State which parasite is depicted.
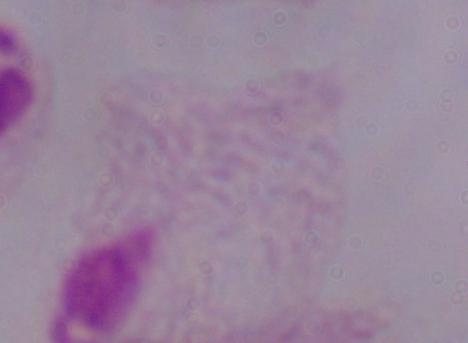

This is a trichomonad.

modality: micrograph
magnification: 1000x